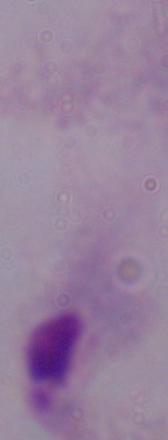
modality = micrograph
identification = trichomonad
magnification = 1000x